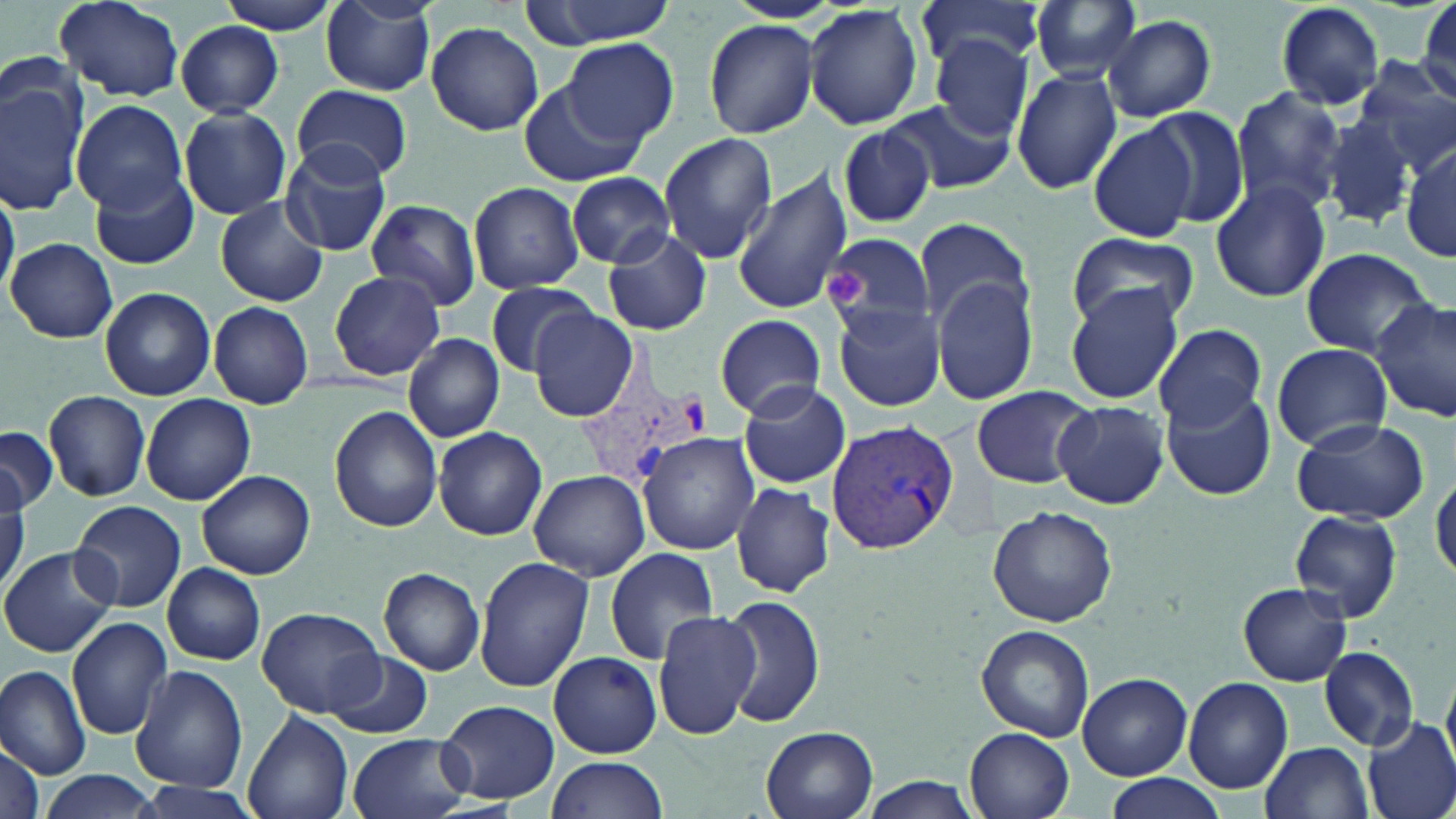

slide-level diagnosis = Plasmodium vivax
stain = May-Grünwald-Giemsa
magnification = 1000x
platelet locations = approximate bounding boxes as [x1, y1, x2, y2] in pixels: [819, 263, 866, 308]
field of view = one of a larger specimen
preparation = thin blood smear
modality = light microscopy
uninfected red blood cell locations = approximate bounding boxes as [x1, y1, x2, y2] in pixels: [217, 0, 342, 35], [520, 0, 681, 47], [320, 1, 437, 94], [1030, 1, 1139, 82], [1275, 1, 1385, 110], [53, 2, 184, 101], [915, 2, 1050, 68], [1405, 2, 1456, 113], [803, 4, 923, 131], [1102, 14, 1215, 122], [703, 19, 817, 138], [425, 20, 544, 135], [176, 21, 285, 117], [561, 37, 678, 147], [930, 37, 1035, 140], [1353, 57, 1456, 172], [1011, 67, 1122, 194], [1, 71, 91, 215], [519, 80, 648, 186], [293, 85, 411, 182], [1230, 88, 1349, 214], [885, 95, 1016, 195], [74, 99, 189, 213], [179, 106, 294, 220], [1140, 106, 1251, 229], [1322, 114, 1415, 230], [1087, 121, 1201, 243], [837, 123, 938, 230], [658, 132, 776, 262], [1400, 139, 1455, 266], [281, 140, 393, 257], [89, 170, 198, 269], [731, 170, 853, 315], [567, 171, 674, 268], [1211, 179, 1330, 303], [468, 181, 585, 293], [0, 186, 20, 302], [214, 197, 330, 307], [365, 197, 481, 311], [913, 218, 1034, 328], [602, 226, 713, 337], [823, 232, 937, 348], [1067, 232, 1198, 329], [6, 238, 116, 342], [1300, 247, 1436, 357], [328, 271, 445, 381], [933, 276, 1040, 405], [485, 281, 596, 376], [1064, 285, 1184, 405], [98, 287, 216, 401], [1371, 299, 1456, 424], [207, 302, 313, 408], [831, 302, 946, 412], [527, 308, 640, 421], [714, 313, 824, 420], [1152, 324, 1267, 428], [403, 333, 505, 442], [1271, 343, 1391, 452], [736, 381, 850, 490], [974, 385, 1096, 490], [1164, 389, 1276, 501], [44, 390, 150, 501], [141, 394, 256, 504], [1052, 400, 1170, 509], [331, 406, 443, 533], [1286, 415, 1428, 523], [0, 427, 57, 514], [434, 427, 547, 540], [638, 431, 761, 556], [195, 469, 316, 579], [529, 470, 651, 582], [1432, 472, 1455, 583], [731, 483, 834, 598], [0, 492, 25, 595], [71, 501, 185, 612], [988, 504, 1116, 626], [1288, 509, 1402, 625], [1, 545, 117, 657], [606, 547, 720, 665], [475, 557, 593, 691], [162, 562, 264, 666], [378, 568, 485, 675], [1238, 582, 1353, 686], [722, 595, 825, 727], [653, 606, 760, 739], [256, 607, 384, 717], [68, 615, 173, 740], [976, 624, 1095, 742], [1319, 648, 1419, 750], [326, 651, 434, 738], [549, 651, 661, 758], [131, 665, 248, 794], [0, 666, 92, 781], [1079, 672, 1191, 780], [1183, 676, 1292, 793], [437, 699, 560, 805], [242, 709, 353, 819], [1363, 715, 1456, 819], [762, 727, 878, 819], [965, 728, 1074, 819], [348, 732, 473, 819], [0, 740, 47, 819], [1261, 741, 1374, 818], [546, 757, 670, 818], [34, 769, 162, 819], [1099, 773, 1230, 819], [859, 778, 987, 817], [132, 779, 262, 819]
Plasmodium vivax-infected red blood cell locations = approximate bounding boxes as [x1, y1, x2, y2] in pixels: [585, 333, 708, 490], [828, 422, 958, 555]
image size = 1456×819 pixels